State which parasite is depicted.
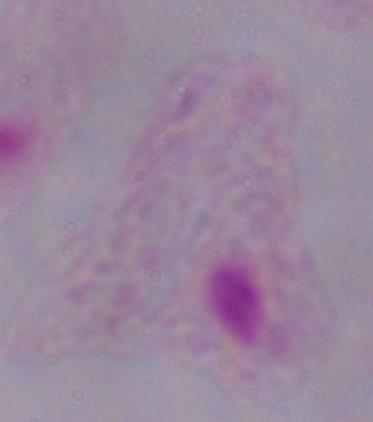

This is a trichomonad.

Summary:
  - Magnification: 1000x
  - Modality: micrograph